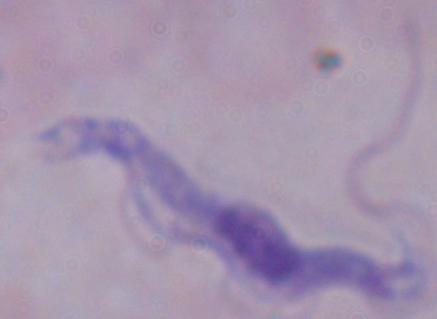
magnification: 1000x
identification: trypanosome
modality: photomicrograph